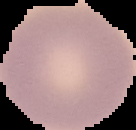
Summary:
  - Image size: 136×130 pixels
  - Result: no malaria parasites detected
  - Preparation: thin blood smear
  - Image type: segmented cell region on a black background